State the blood parasite species.
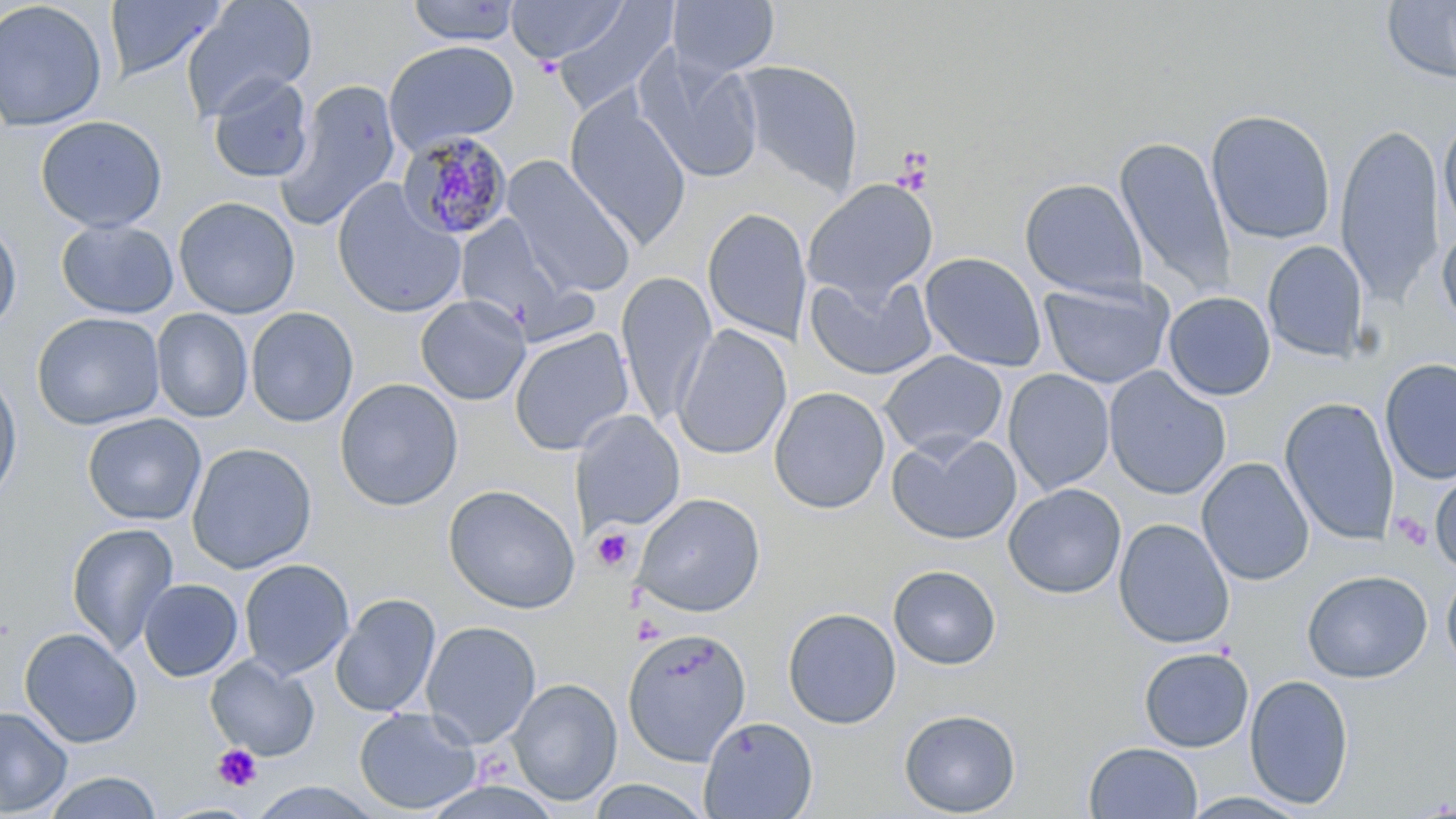
Plasmodium malariae.

Summary:
  - Coordinate format: approximate bounding boxes as (x1,y1)-(x2,y2) corner pairs in pixels
  - Plasmodium malariae-infected red blood cell locations: (397,130)-(514,241)
  - Platelet locations: (891,149)-(935,193), (1390,512)-(1434,552), (590,528)-(635,571), (212,744)-(263,792)
  - Uninfected red blood cell locations: (104,0)-(227,83), (507,0)-(628,64), (667,0)-(780,79), (1381,0)-(1456,85), (0,1)-(110,132), (181,1)-(317,121), (405,1)-(523,46), (552,3)-(677,116), (383,40)-(519,154), (633,50)-(764,183), (734,60)-(865,195), (207,73)-(315,183), (275,79)-(403,233), (565,96)-(692,248), (1205,109)-(1336,245), (1438,114)-(1456,239), (35,115)-(167,233), (1335,121)-(1444,306), (1115,136)-(1237,297), (501,156)-(636,297), (1019,178)-(1147,299), (804,179)-(938,302), (331,181)-(467,319), (173,196)-(300,319), (702,207)-(813,344), (455,213)-(594,343), (0,219)-(22,333), (56,219)-(179,319), (1437,221)-(1456,333), (1262,241)-(1368,362), (920,252)-(1047,372), (616,272)-(718,426), (806,274)-(937,380), (1038,279)-(1175,389), (1163,291)-(1276,401), (415,294)-(531,406), (245,307)-(358,427), (151,308)-(253,423), (32,312)-(166,431), (674,324)-(792,461), (509,328)-(634,456), (879,350)-(1008,457), (1380,358)-(1456,484), (1003,368)-(1115,495), (1103,368)-(1231,500), (0,369)-(23,505), (335,378)-(463,511), (769,386)-(890,514), (1280,396)-(1400,546), (572,411)-(684,533), (82,413)-(206,525), (886,430)-(1022,545), (186,442)-(317,574), (1196,457)-(1314,586), (1430,470)-(1456,575), (1003,482)-(1127,599), (443,484)-(580,614), (633,493)-(766,617), (1113,518)-(1235,650), (65,522)-(179,655), (239,559)-(355,679), (888,564)-(1001,670), (1441,568)-(1456,675), (1302,569)-(1432,683), (138,578)-(243,682), (330,593)-(440,717), (782,607)-(902,729), (421,620)-(541,748), (19,627)-(142,748), (622,627)-(752,765), (1139,647)-(1254,752), (205,655)-(319,761), (1244,674)-(1354,810), (508,677)-(622,806), (0,706)-(72,816), (353,707)-(481,815), (898,708)-(1021,816), (698,716)-(818,818), (1084,741)-(1203,818), (40,770)-(164,819), (586,777)-(713,818), (1180,791)-(1313,818)
  - Preparation: thin blood smear
  - Stain: May-Grünwald-Giemsa
  - Image size: 1456×819 pixels
  - Modality: optical microscopy
  - Field of view: one of a larger specimen
  - Magnification: 1000x